Point out each leukocyte.
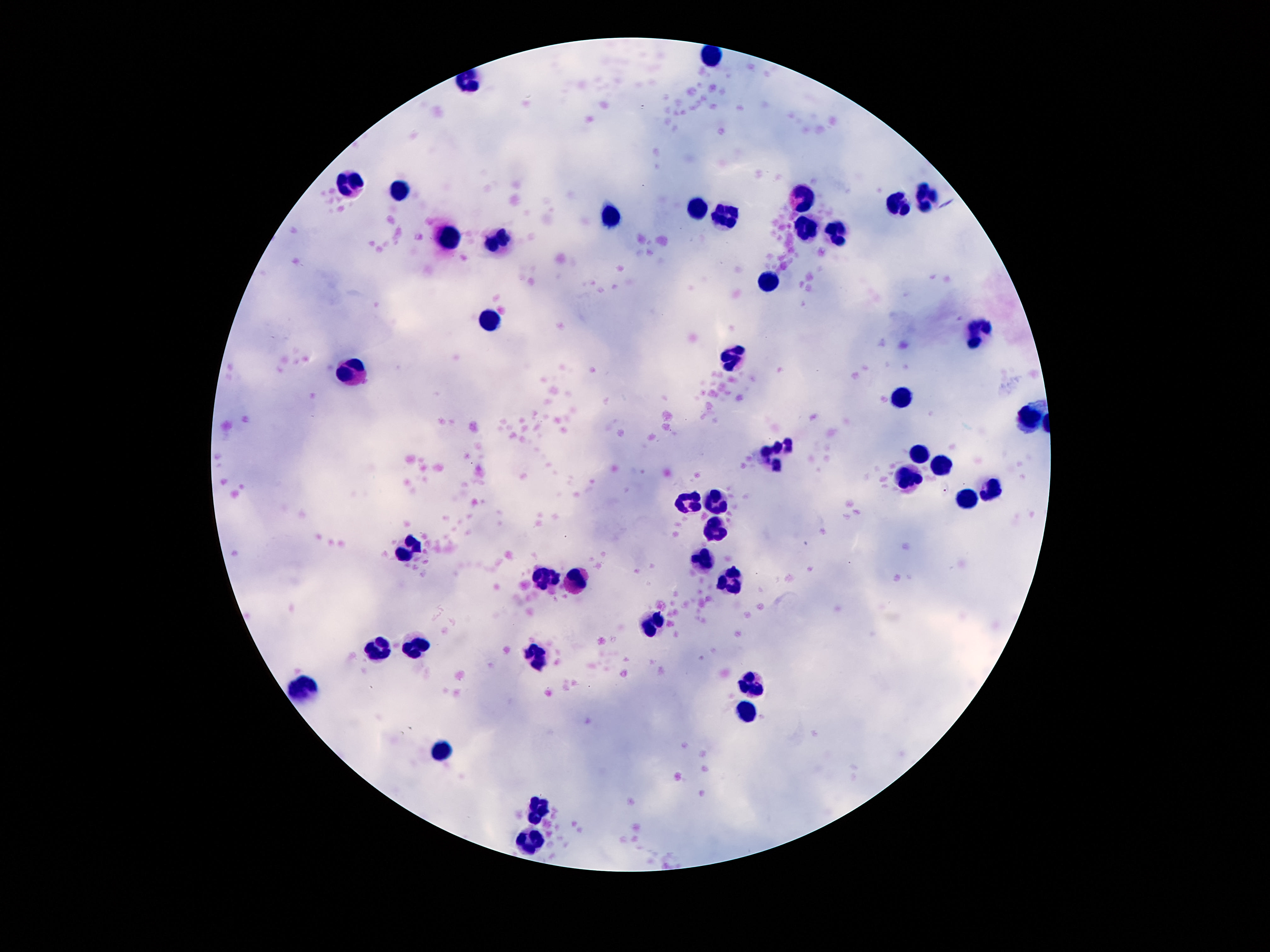
Approximate object centers, in pixels from the top-left corner.
Leukocytes: (x=349, y=184), (x=399, y=192), (x=924, y=197), (x=799, y=199), (x=896, y=204), (x=697, y=210), (x=610, y=213), (x=724, y=219), (x=803, y=231), (x=833, y=235), (x=497, y=236), (x=449, y=240), (x=767, y=282), (x=490, y=319), (x=976, y=329), (x=731, y=356), (x=354, y=372), (x=899, y=401), (x=1028, y=415), (x=915, y=454), (x=774, y=456), (x=940, y=466), (x=910, y=478), (x=991, y=487), (x=965, y=502), (x=687, y=503), (x=719, y=503), (x=713, y=529), (x=411, y=553), (x=704, y=560), (x=547, y=580), (x=576, y=583), (x=729, y=583), (x=651, y=619), (x=417, y=645), (x=377, y=648), (x=533, y=658), (x=749, y=683), (x=302, y=688), (x=746, y=713), (x=442, y=754), (x=538, y=810), (x=529, y=843).

patient_malaria_status: uninfected
preparation: thick peripheral-blood smear
stain: Giemsa
capture: smartphone camera through the microscope eyepiece
field_of_view: one from this slide
image_size: 1270×952 pixels
magnification: 100x